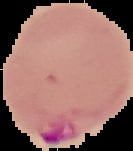
The area outside the segmented cell region is set to black. Image is 133×151 pixels. Result: malaria parasites detected. From a thin blood smear.